State the blood parasite species.
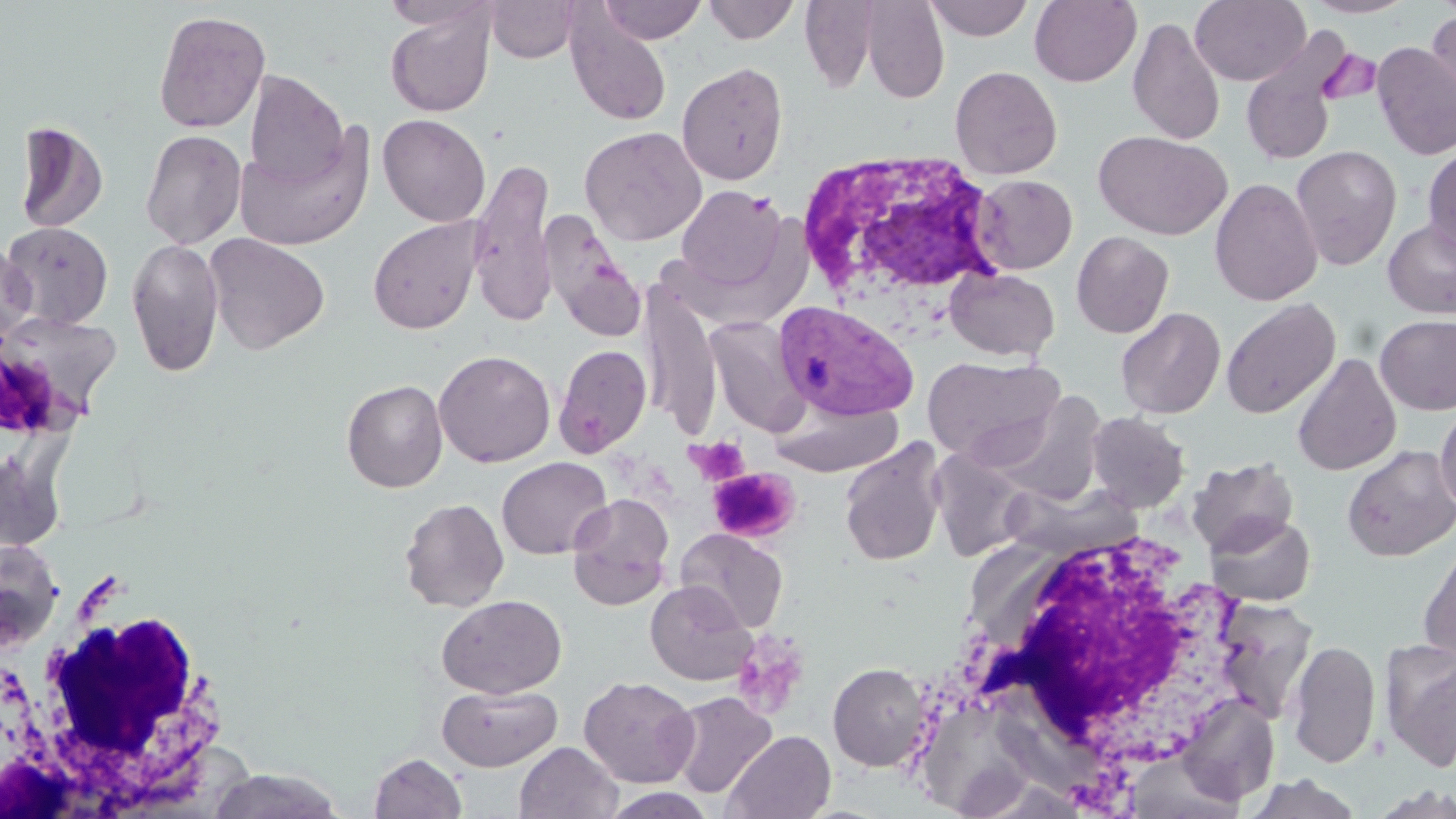

Plasmodium vivax.

Summary:
  - Coordinate format: approximate bounding boxes as (x1,y1)-(x2,y2) corner pairs in pixels
  - Uninfected red blood cell locations: (485,0)-(582,62), (597,0)-(707,44), (703,0)-(800,44), (924,0)-(1035,41), (1029,0)-(1142,87), (1190,0)-(1310,85), (1301,0)-(1417,18), (799,1)-(882,93), (860,1)-(949,104), (384,6)-(495,118), (153,9)-(271,133), (1426,10)-(1456,117), (566,13)-(672,127), (1127,17)-(1226,146), (1239,29)-(1352,166), (1372,42)-(1456,161), (677,62)-(788,185), (950,65)-(1062,179), (244,70)-(348,187), (377,113)-(490,228), (14,121)-(108,234), (579,125)-(707,245), (234,126)-(373,252), (140,128)-(247,249), (1093,130)-(1232,240), (1422,144)-(1456,258), (1290,145)-(1402,270), (468,156)-(559,327), (971,174)-(1077,274), (1209,178)-(1323,306), (675,185)-(788,293), (540,210)-(648,343), (368,216)-(484,335), (1382,218)-(1456,319), (1,221)-(114,329), (1071,231)-(1174,338), (204,233)-(330,354), (126,237)-(224,377), (0,241)-(35,343), (945,267)-(1059,361), (641,288)-(722,438), (1220,298)-(1340,419), (1115,307)-(1225,419), (0,313)-(119,432), (1374,314)-(1456,415), (704,316)-(809,437), (555,344)-(652,457), (434,349)-(556,467), (1292,353)-(1401,476), (922,356)-(1065,466), (341,379)-(448,493), (992,392)-(1107,505), (768,398)-(903,477), (1434,403)-(1456,514), (1086,411)-(1190,513), (839,439)-(947,567), (1342,445)-(1456,562), (0,448)-(67,553), (929,448)-(1033,562), (1188,456)-(1299,556), (496,457)-(612,560), (1001,481)-(1141,561), (567,493)-(675,610), (399,497)-(509,612), (1205,513)-(1315,607), (676,528)-(788,633), (0,539)-(63,651), (1418,543)-(1456,668), (646,581)-(758,686), (437,594)-(566,698), (1215,599)-(1318,723), (1288,639)-(1379,769), (1381,639)-(1456,771), (828,662)-(932,771), (579,675)-(700,788), (437,684)-(563,771), (668,691)-(776,798), (1174,693)-(1280,807), (722,729)-(836,819), (514,741)-(621,819), (369,752)-(467,819), (207,768)-(346,818), (1245,775)-(1363,818), (1368,783)-(1456,818), (601,788)-(717,818)
  - Plasmodium vivax-infected red blood cell locations: (773,300)-(919,423)
  - White blood cell locations: (793,150)-(1009,308), (946,521)-(1256,800), (13,602)-(231,812)
  - Platelet locations: (1317,48)-(1381,107), (688,436)-(750,487), (708,467)-(798,543), (732,629)-(811,719)
  - Field of view: one of a larger specimen
  - Stain: May-Grünwald-Giemsa
  - Image size: 1456×819 pixels
  - Modality: optical microscopy
  - Magnification: 1000x
  - Preparation: thin blood film